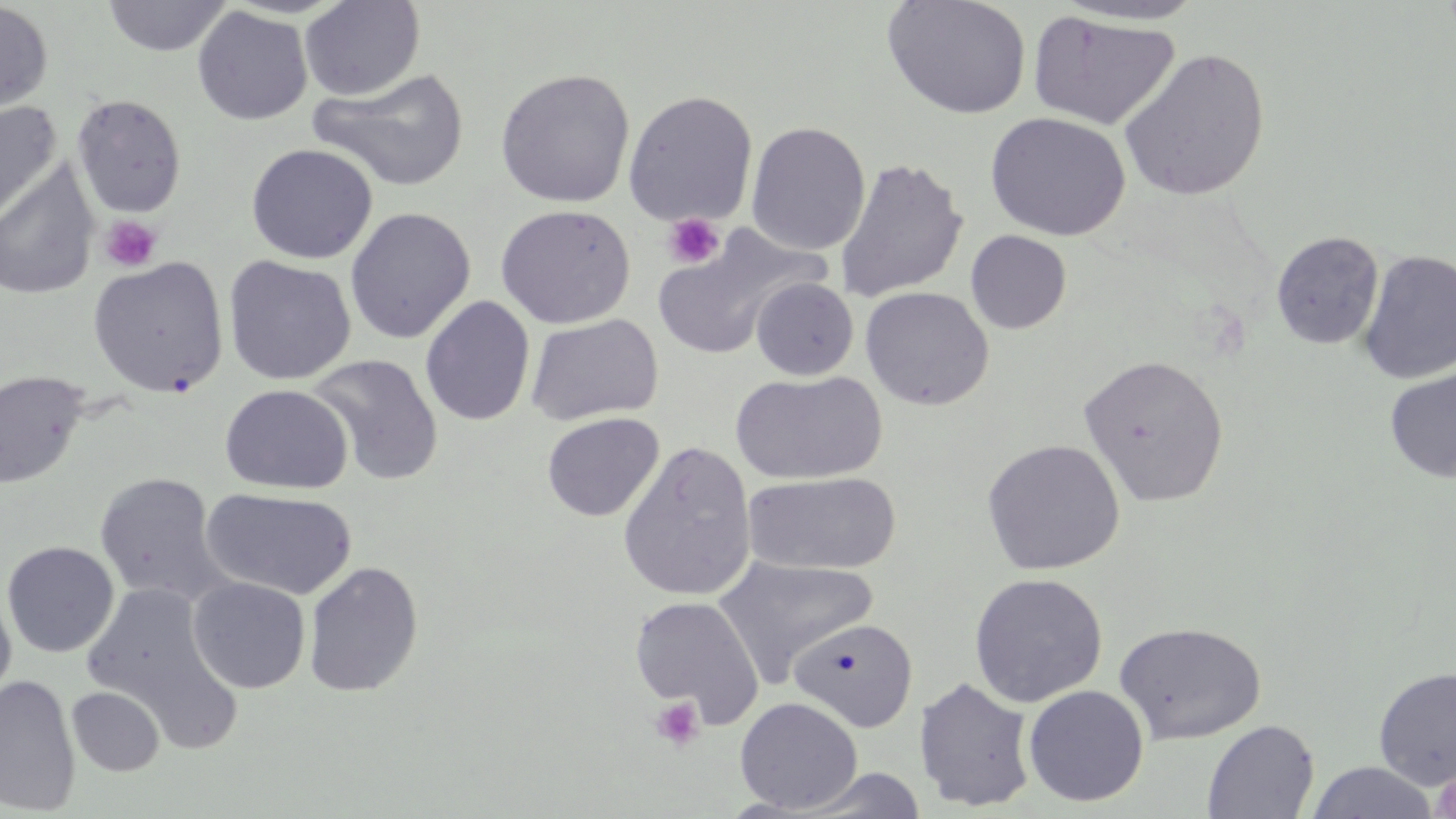
Approximate bounding boxes as (x1, y1, x2, y2) in pixels. Uninfected red blood cell locations: (102, 0, 232, 56), (299, 0, 424, 101), (881, 0, 1033, 120), (0, 1, 53, 113), (1052, 1, 1209, 26), (192, 6, 313, 126), (1027, 11, 1182, 131), (1119, 47, 1270, 202), (494, 67, 636, 208), (310, 68, 470, 193), (622, 90, 759, 228), (71, 94, 187, 217), (0, 100, 62, 225), (985, 112, 1131, 241), (746, 121, 870, 256), (245, 143, 378, 264), (834, 156, 968, 303), (0, 162, 99, 300), (494, 204, 636, 329), (345, 207, 476, 344), (651, 223, 824, 360), (965, 230, 1072, 334), (1270, 231, 1384, 350), (1358, 250, 1456, 384), (223, 255, 357, 385), (88, 256, 229, 397), (751, 277, 858, 380), (859, 286, 994, 410), (420, 295, 535, 426), (526, 313, 663, 426), (308, 354, 443, 486), (1078, 354, 1229, 507), (1384, 368, 1456, 483), (0, 370, 90, 490), (730, 370, 887, 485), (220, 384, 353, 495), (542, 412, 663, 521), (981, 439, 1125, 575), (617, 440, 757, 601), (744, 471, 902, 575), (94, 472, 227, 605), (202, 487, 358, 600), (2, 541, 120, 658), (713, 555, 878, 685), (303, 560, 423, 698), (969, 572, 1108, 707), (187, 576, 311, 694), (82, 581, 239, 740), (0, 582, 16, 712), (629, 595, 764, 728), (788, 618, 918, 732), (1114, 621, 1266, 744), (1373, 666, 1456, 790), (0, 673, 80, 815), (914, 676, 1037, 812), (1023, 685, 1149, 807), (66, 686, 165, 776), (734, 696, 863, 813), (1202, 719, 1319, 818), (1305, 761, 1440, 818), (795, 768, 930, 818). Platelet locations: (662, 213, 725, 269), (100, 215, 162, 272), (651, 697, 705, 751), (1432, 766, 1456, 819). Slide-level diagnosis: negative for blood parasites. May-Grünwald-Giemsa stain. Captured at 1000x magnification. Image is 1456×819 pixels. Thin blood smear. One field of a larger specimen. Optical microscopy.